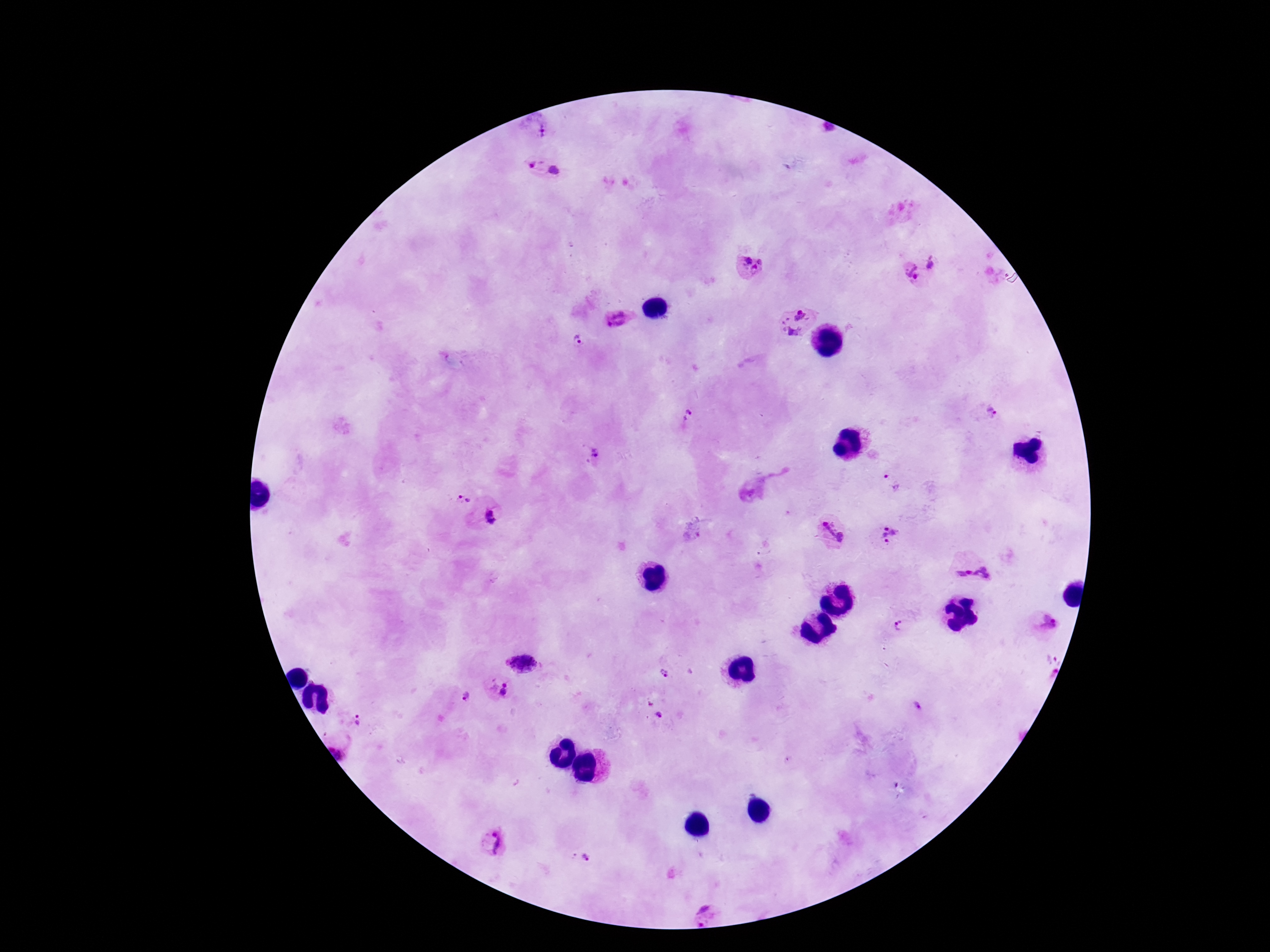

Approximate centers as [x, y] in pixels.
Summary:
  - Plasmodium parasite locations: [542, 169], [934, 262], [752, 265], [912, 272], [618, 318], [794, 322], [578, 340], [994, 414], [688, 417], [593, 452], [889, 483], [464, 501], [493, 516], [832, 529], [890, 535], [973, 574], [1049, 623], [899, 625], [521, 663], [665, 672], [500, 689], [465, 697], [660, 717], [359, 720], [340, 747], [494, 843], [587, 858], [707, 914]
  - Image size: 1270×952 pixels
  - Field of view: single
  - Magnification: 100x
  - Stain: Giemsa
  - Patient malaria status: positive
  - Preparation: thick blood film
  - Capture: smartphone camera through the microscope eyepiece